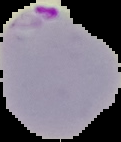
From a thin blood film. Image is 121×142 pixels. The area outside the segmented cell region is set to black. Malaria status: parasitized.